Assess this cell for malaria.
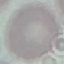

Uninfected.

capture = smartphone through the microscope eyepiece
image type = automatically extracted cell patch, resized to 64 × 64 pixels
preparation = thin smear
stain = Giemsa